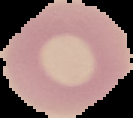

malaria status = uninfected
preparation = thin blood film
image type = segmented cell region with the area outside set to black
image size = 133×118 pixels